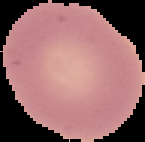
From a thin blood smear. Segmented cell region on a black background. Result: negative for Plasmodium parasites. Image is 145×142 pixels.